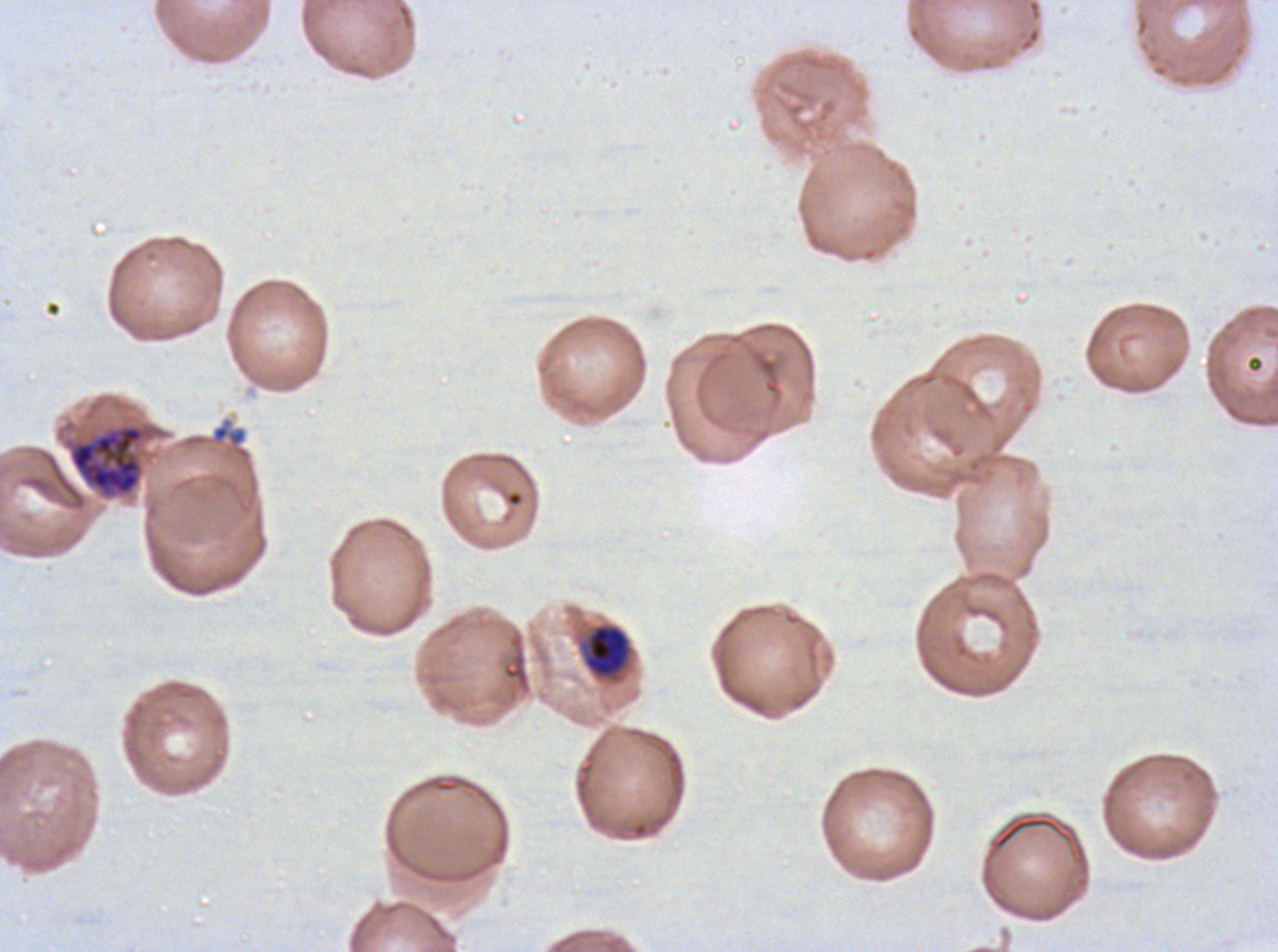 Approximate bounding boxes as (x1, y1, x2, y2) in pixels. Early schizont locations: (64, 423, 149, 499). Mid trophozoite locations: (584, 625, 629, 677). Image is 1278×952 pixels. Giemsa stain. One sub-image of a larger composite. P. falciparum from a patient in The Gambia, cultured ex vivo for 24 to 48 hours. Thin blood smear. Life-cycle stages observed: mid trophozoite, early schizont.